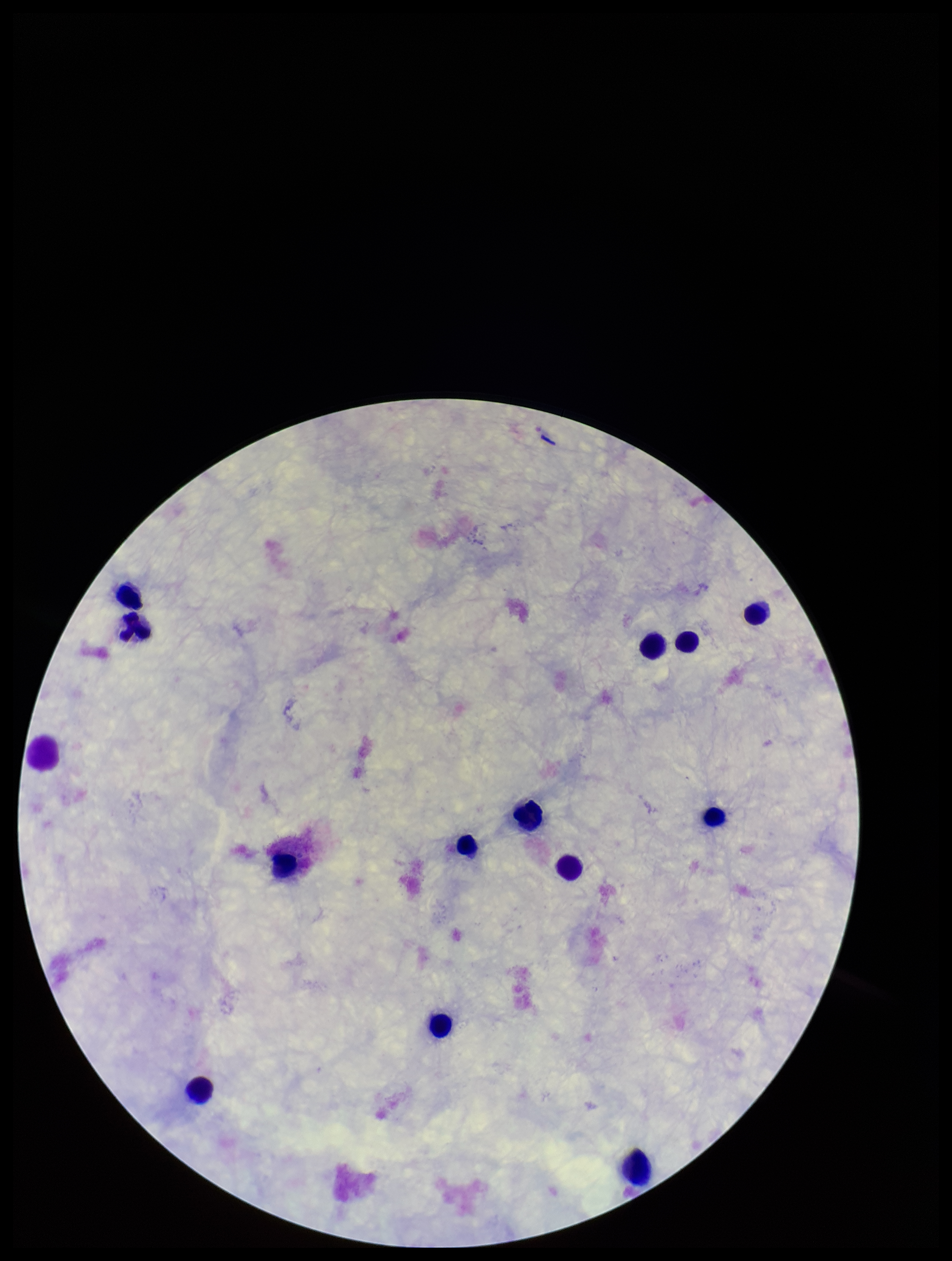
Summary:
  - Field of view: single
  - Plasmodium parasites: none detected
  - Preparation: thick smear
  - Parasite count: 0
  - Stain: Giemsa
  - Patient malaria status: negative
  - Capture: smartphone photograph through the microscope eyepiece
  - Leukocyte count: 14
  - Image size: 952×1261 pixels